Report the malaria status of this cell.
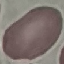
It is uninfected.

Automatically extracted cell patch, resized to 64 × 64 pixels. Giemsa stain. Thin smear of blood. Acquired by smartphone through the microscope eyepiece.